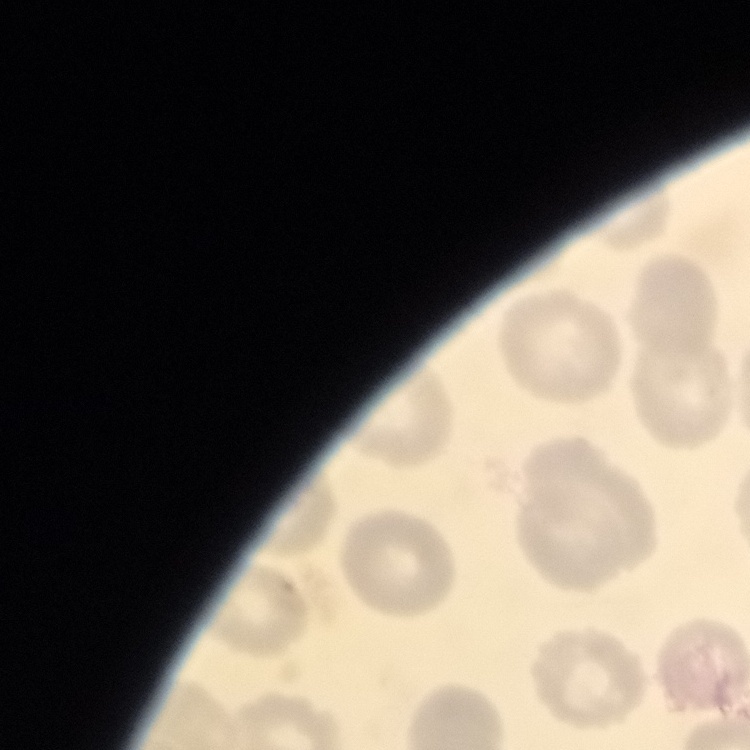
Summary:
  - Erythrocyte morphology: no rouleaux formation
  - Image type: one tile cut from a larger photomicrograph
  - Preparation: thin peripheral smear
  - Stain: Field's or Giemsa